Classify this cell by malaria status.
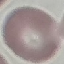

It is uninfected.

Summary:
  - Image type: cell patch, automatically extracted from a larger field of view and resized to 64 × 64 pixels
  - Preparation: thin blood film
  - Stain: Giemsa
  - Capture: smartphone through the microscope eyepiece